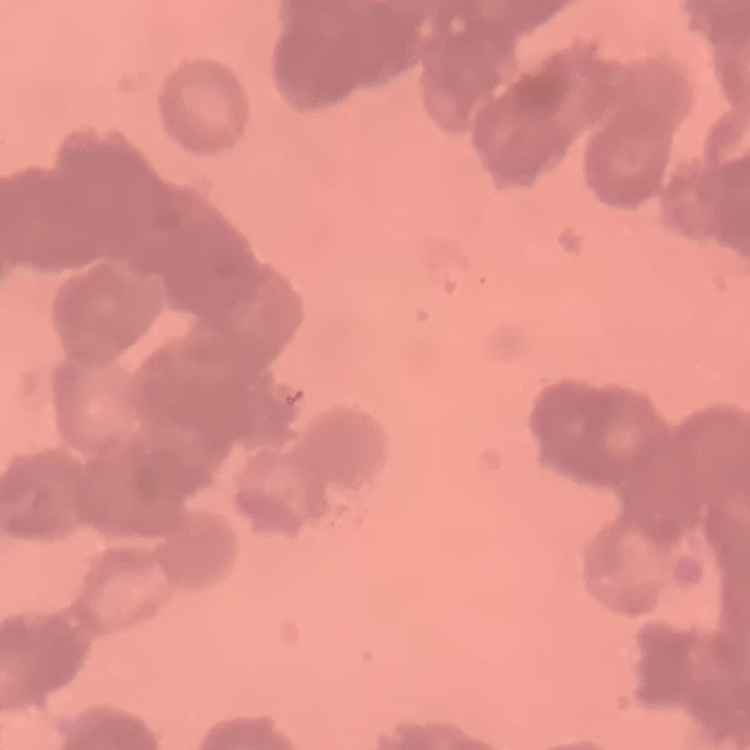
Summary:
  - Erythrocyte morphology: rouleaux formation
  - Stain: Field's or Giemsa
  - Image type: one tile cut from a larger photomicrograph
  - Preparation: thin blood film